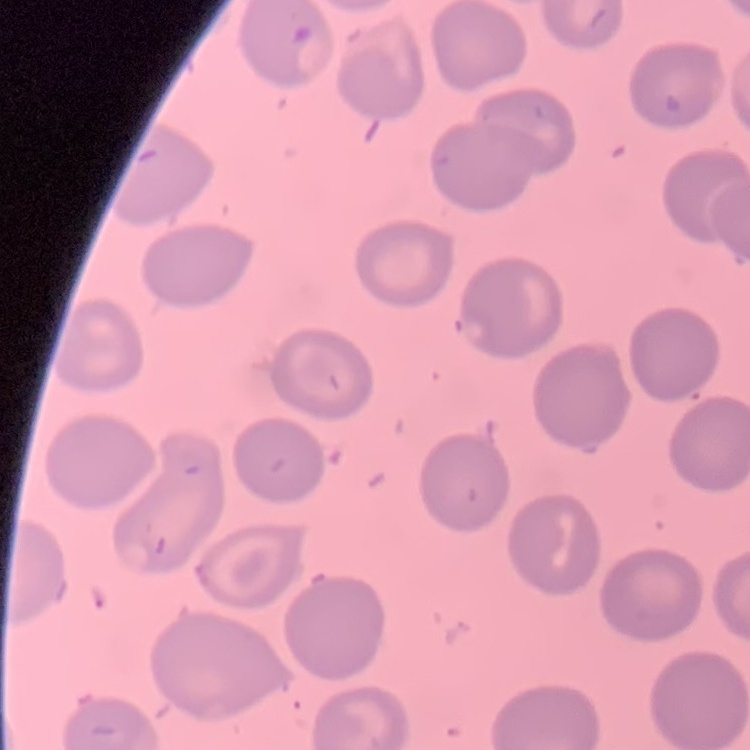

erythrocyte_morphology: no rouleaux formation
preparation: thin blood smear
stain: Field's or Giemsa
image_type: one tile cut from a larger photomicrograph